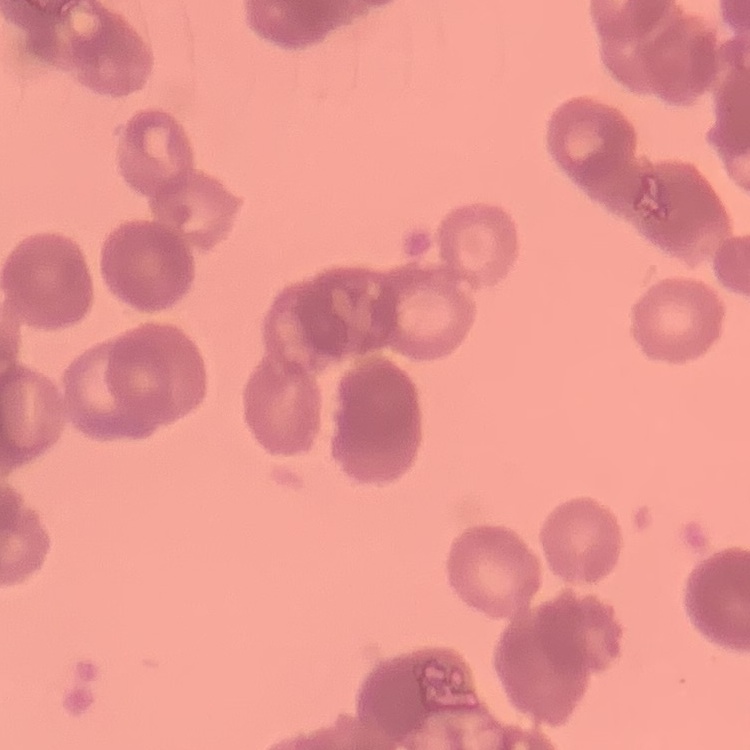

erythrocyte morphology = rouleaux formation
image type = one tile cut from a larger photomicrograph
preparation = thin blood smear
stain = Field's or Giemsa